Classify this cell by malaria status.
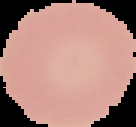
Uninfected.

Summary:
  - Image type: segmented cell region with the area outside set to black
  - Image size: 136×127 pixels
  - Preparation: thin blood smear